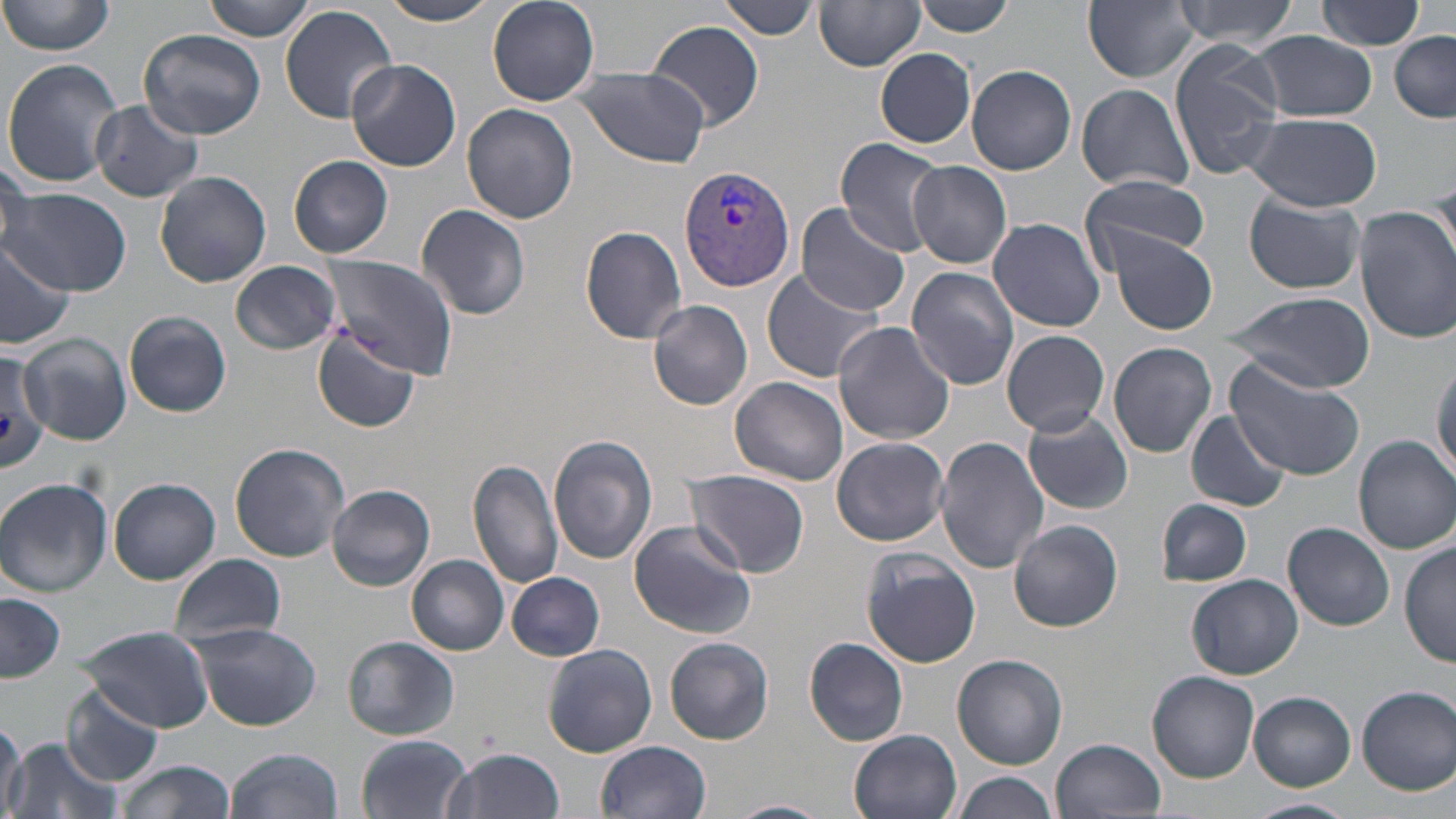

Approximate bounding boxes as [x1, y1, x2, y2] in pixels. Plasmodium vivax-infected red blood cell locations: [679, 165, 796, 292]. Uninfected red blood cell locations: [2, 0, 115, 56], [201, 0, 319, 41], [379, 0, 505, 26], [487, 0, 600, 105], [913, 0, 1015, 37], [1084, 0, 1199, 83], [1174, 0, 1304, 47], [1316, 0, 1427, 51], [717, 1, 822, 40], [814, 2, 926, 71], [279, 6, 398, 122], [649, 22, 764, 130], [139, 29, 265, 139], [1252, 30, 1379, 121], [1390, 30, 1455, 121], [1169, 42, 1286, 180], [874, 48, 976, 148], [2, 59, 124, 187], [345, 60, 461, 172], [966, 65, 1077, 175], [572, 66, 709, 166], [1075, 83, 1195, 195], [89, 100, 205, 203], [462, 104, 579, 224], [1246, 112, 1382, 212], [833, 139, 949, 255], [1, 154, 31, 254], [289, 155, 393, 257], [907, 160, 1011, 269], [155, 170, 272, 287], [1427, 171, 1456, 272], [1082, 173, 1209, 268], [0, 189, 132, 296], [1244, 194, 1366, 295], [793, 202, 914, 318], [415, 204, 531, 322], [1355, 208, 1456, 341], [989, 217, 1105, 332], [580, 226, 688, 344], [1111, 234, 1218, 335], [0, 235, 75, 347], [320, 255, 458, 380], [231, 261, 342, 356], [905, 266, 1018, 391], [761, 268, 886, 384], [1223, 292, 1373, 391], [649, 300, 753, 411], [124, 311, 230, 416], [833, 321, 955, 445], [311, 327, 423, 433], [1001, 329, 1110, 437], [20, 332, 132, 446], [1107, 341, 1219, 459], [0, 346, 49, 470], [1226, 357, 1364, 480], [1430, 358, 1456, 478], [732, 376, 849, 488], [1186, 408, 1290, 513], [1024, 409, 1132, 515], [1354, 435, 1455, 553], [549, 436, 658, 565], [934, 436, 1051, 575], [831, 437, 950, 546], [230, 443, 351, 563], [469, 457, 564, 590], [685, 471, 809, 577], [108, 477, 221, 584], [0, 478, 113, 596], [328, 484, 435, 592], [1156, 498, 1251, 587], [627, 519, 759, 640], [1009, 520, 1122, 633], [1283, 521, 1395, 631], [1401, 540, 1455, 669], [860, 548, 983, 668], [408, 554, 510, 655], [169, 555, 286, 648], [507, 572, 605, 661], [1187, 573, 1305, 679], [0, 593, 65, 684], [191, 622, 322, 731], [75, 623, 216, 733], [344, 636, 458, 742], [804, 636, 909, 746], [664, 637, 774, 744], [543, 644, 658, 757], [952, 653, 1068, 769], [1148, 670, 1259, 782], [1356, 685, 1456, 794], [63, 686, 167, 786], [1248, 692, 1355, 790], [0, 717, 26, 819], [849, 730, 963, 819], [355, 734, 473, 818], [8, 735, 123, 819], [1051, 737, 1166, 818], [596, 739, 713, 819], [227, 748, 343, 819], [443, 749, 566, 819], [115, 758, 236, 819], [954, 772, 1059, 819], [1244, 797, 1358, 819], [723, 799, 830, 819]. Slide-level diagnosis: Plasmodium vivax. Thin blood film. Image is 1456×819 pixels. May-Grünwald-Giemsa stain. Single field of view. Captured at 1000x magnification. Light microscopy.